Report the malaria status of this cell.
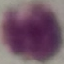

It is uninfected.

Automatically extracted cell patch, resized to 64 × 64 pixels. Acquired by smartphone through the microscope eyepiece. Giemsa-stained preparation. Thin smear of blood.